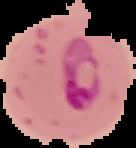

{
  "image_size": "136×148 pixels",
  "preparation": "thin blood smear",
  "image_type": "cell region segmented out of the field of view; surrounding area masked to black",
  "malaria_status": "parasitized"
}